Assess this cell for malaria.
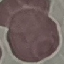
Uninfected.

capture = smartphone camera at the microscope eyepiece
preparation = thin smear
stain = Giemsa
image type = automatically extracted cell patch, resized to 64 × 64 pixels